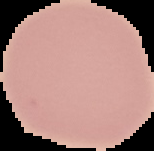

Image is 154×151 pixels. Malaria status: uninfected. From a thin blood smear. Segmented cell region on a black background.